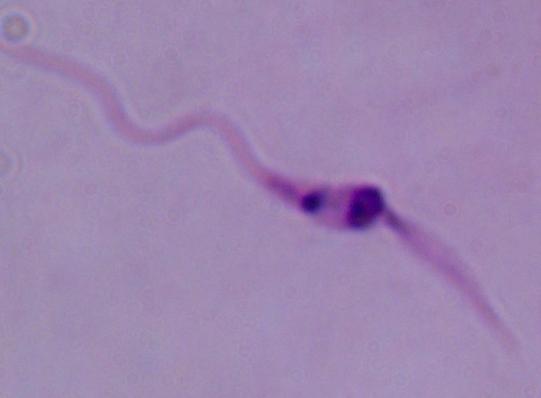 Micrograph. 1000x magnification. A Leishmania parasite is seen.